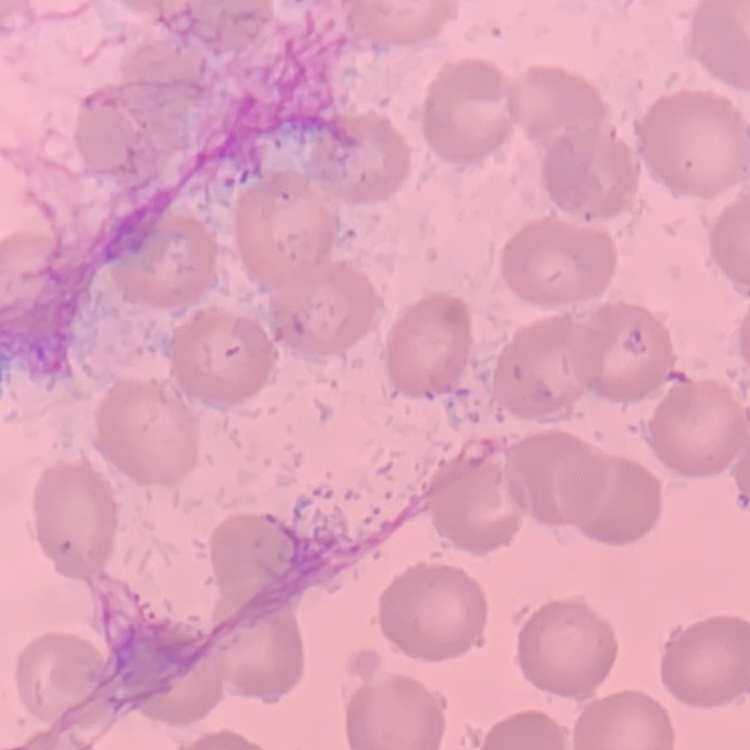

erythrocyte morphology = no rouleaux formation
stain = Field's or Giemsa
preparation = thin blood film
image type = square crop of a larger photomicrograph